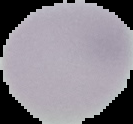

result = no Plasmodium parasites seen
image size = 133×124 pixels
preparation = thin blood smear
image type = segmented cell region on a black background